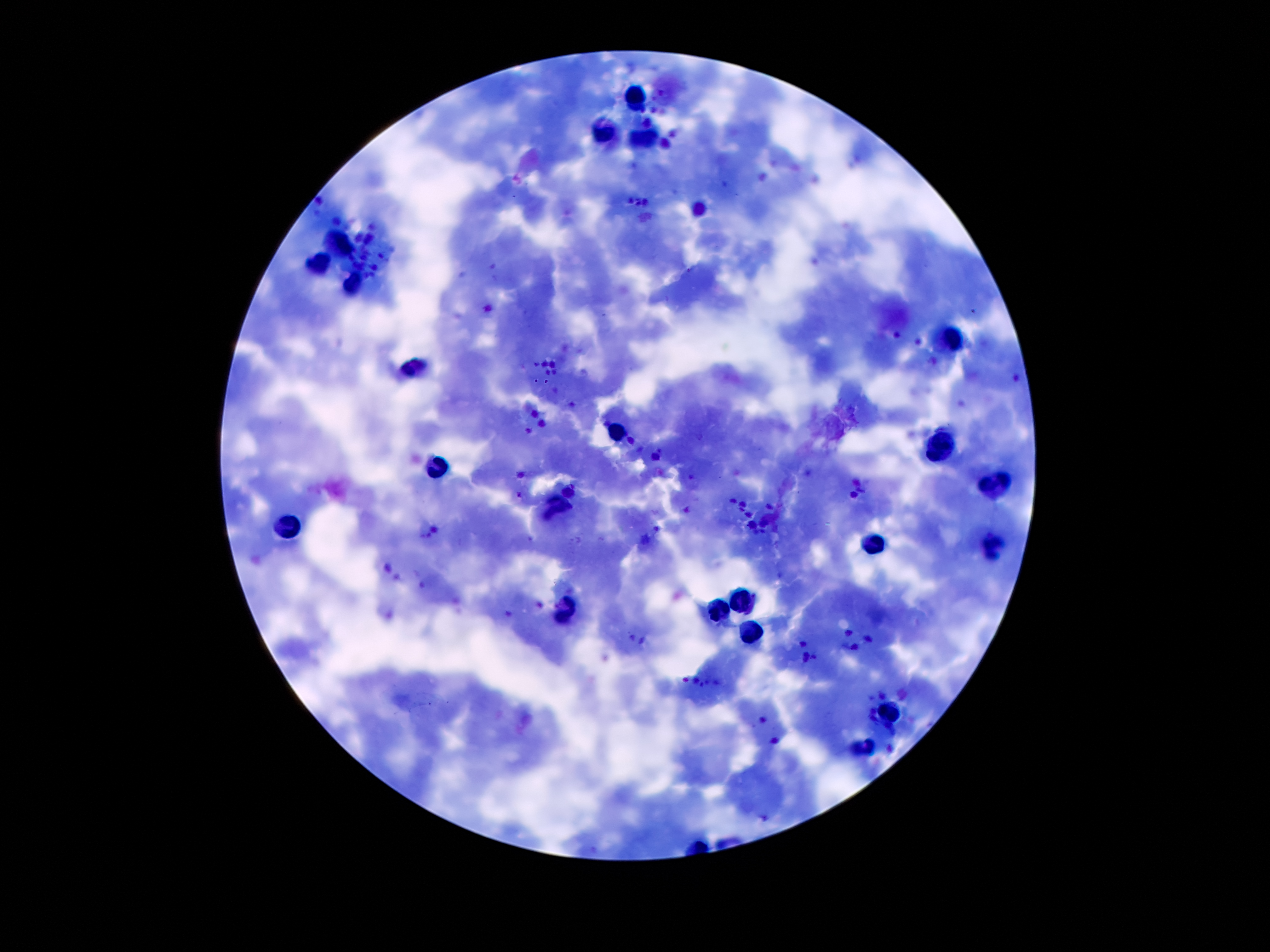 Patient malaria status: positive for Plasmodium falciparum. Image is 1270×952 pixels. Photographed through the microscope eyepiece with a smartphone camera. Thick blood smear. 100x magnification. Giemsa stain. Single field of view.